State which parasite is depicted.
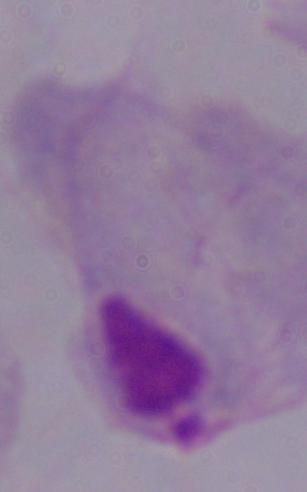
This is a trichomonad.

Micrograph. 1000x magnification.